Assess this cell for malaria.
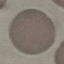

It is uninfected.

Summary:
  - Capture: smartphone camera at the microscope eyepiece
  - Stain: Giemsa
  - Preparation: thin smear
  - Image type: cell patch, automatically extracted from a larger field of view and resized to 64 × 64 pixels